Report the malaria status of this cell.
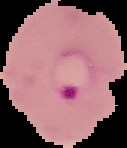

It is parasitized.

Summary:
  - Preparation: thin blood smear
  - Image size: 127×148 pixels
  - Image type: cell region segmented out of the field of view; surrounding area masked to black